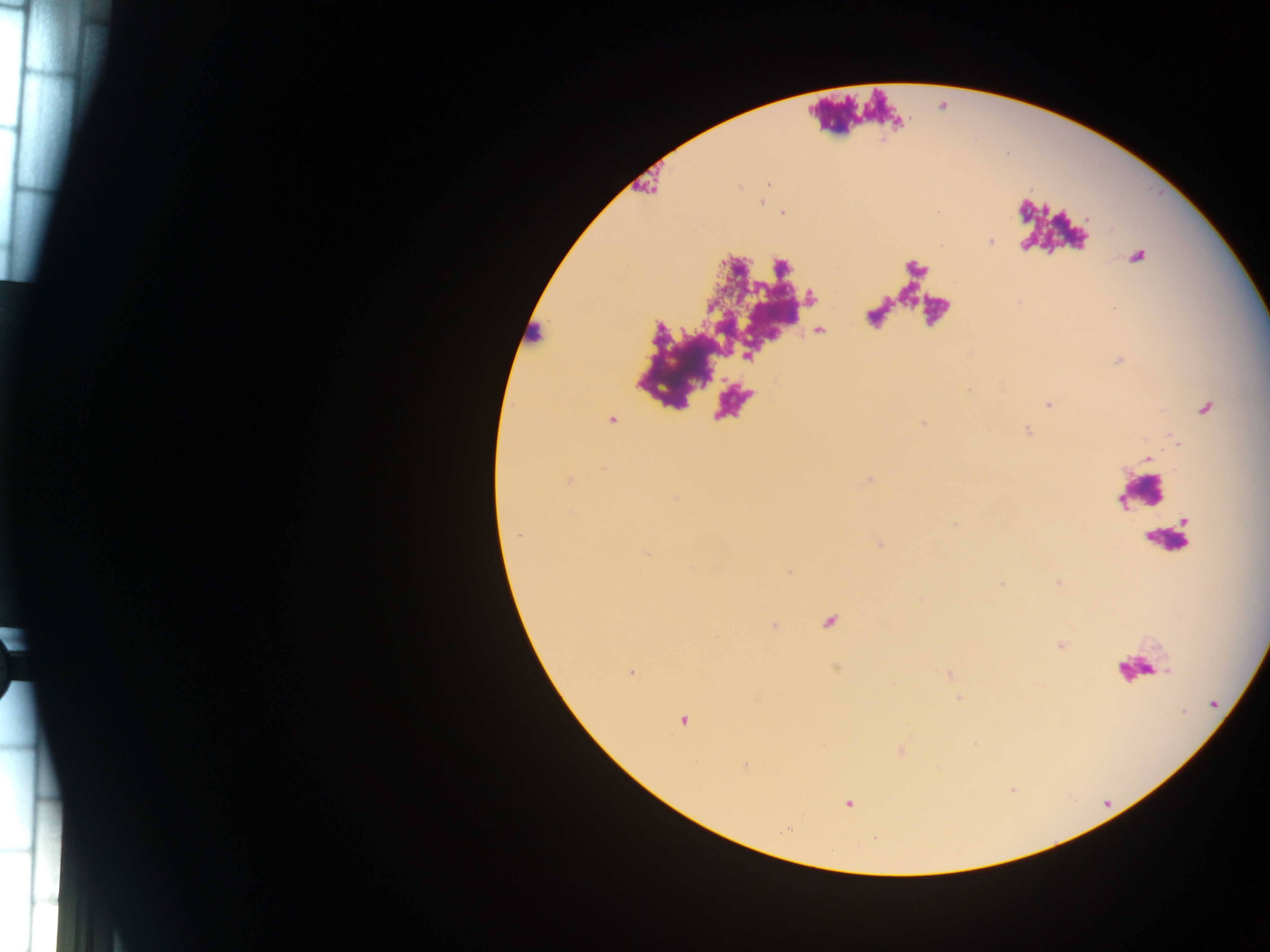

Approximate centers as [x, y] in pixels.
Summary:
  - Leukocyte locations: [534, 334], [1142, 492], [1167, 543], [1139, 667]
  - Plasmodium parasite locations: [769, 184], [761, 202], [782, 213], [991, 242], [1137, 257], [1049, 405], [1206, 409], [1147, 457], [518, 537], [631, 673], [683, 720], [746, 766], [849, 803]
  - Preparation: thick blood smear
  - Capture: mobile-phone photograph through a microscope
  - Country: Ghana
  - Image size: 1270×952 pixels
  - Field of view: single